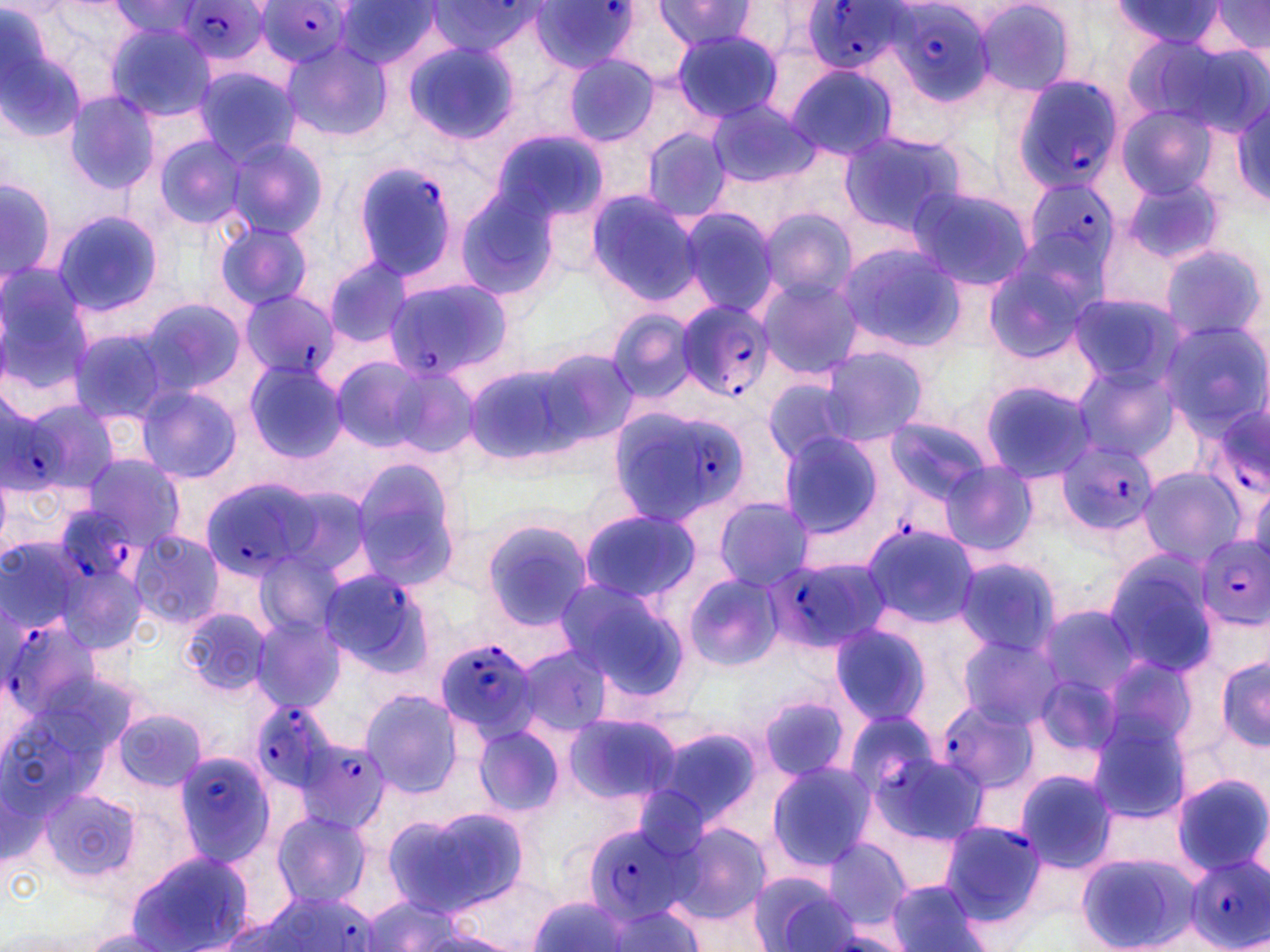

Summary:
  - Coordinate format: approximate bounding boxes as [x1, y1, x2, y2] in pixels
  - Plasmodium falciparum-infected red blood cell locations: [531, 0, 639, 72], [174, 1, 272, 68], [255, 1, 356, 67], [427, 1, 542, 57], [800, 1, 909, 76], [888, 2, 997, 105], [1010, 76, 1123, 196], [352, 160, 460, 286], [1019, 180, 1118, 279], [383, 279, 510, 382], [238, 289, 338, 383], [673, 299, 773, 400], [17, 398, 122, 495], [1222, 400, 1270, 504], [613, 404, 753, 527], [1055, 439, 1159, 535], [197, 478, 326, 582], [55, 506, 136, 583], [1197, 536, 1270, 626], [761, 557, 884, 657], [318, 567, 434, 677], [0, 612, 105, 735], [434, 638, 542, 738], [936, 696, 1035, 800], [252, 699, 339, 793], [849, 713, 937, 800], [295, 735, 390, 835], [174, 749, 279, 869], [941, 820, 1046, 924], [583, 823, 693, 921], [1185, 854, 1270, 949], [242, 891, 377, 952]
  - Uninfected red blood cell locations: [973, 0, 1078, 96], [1108, 0, 1224, 56], [111, 1, 210, 44], [334, 1, 436, 70], [653, 1, 758, 52], [1202, 1, 1270, 57], [0, 5, 88, 141], [604, 5, 700, 87], [105, 22, 218, 121], [671, 29, 783, 124], [1169, 38, 1270, 137], [402, 39, 519, 143], [281, 42, 392, 141], [560, 53, 663, 147], [785, 63, 898, 162], [192, 66, 301, 164], [64, 90, 161, 195], [1227, 95, 1270, 208], [707, 99, 820, 186], [1115, 104, 1218, 201], [638, 125, 735, 226], [490, 128, 607, 229], [837, 129, 967, 234], [157, 135, 246, 228], [226, 138, 326, 238], [1117, 171, 1228, 268], [0, 177, 57, 279], [905, 185, 1034, 292], [453, 186, 565, 301], [584, 189, 704, 305], [672, 206, 781, 317], [757, 208, 858, 304], [53, 211, 162, 316], [216, 222, 314, 311], [833, 243, 965, 355], [1160, 244, 1266, 343], [982, 249, 1098, 365], [323, 256, 412, 348], [0, 264, 94, 394], [755, 276, 864, 380], [1065, 292, 1182, 388], [138, 297, 246, 396], [605, 310, 703, 404], [1156, 320, 1269, 432], [66, 327, 174, 428], [532, 344, 642, 450], [816, 347, 929, 446], [329, 356, 429, 453], [244, 360, 349, 462], [465, 360, 586, 466], [381, 362, 482, 460], [1071, 364, 1181, 463], [761, 375, 860, 468], [980, 379, 1099, 482], [135, 384, 243, 484], [882, 416, 992, 507], [777, 433, 887, 538], [79, 453, 186, 549], [348, 458, 465, 592], [940, 461, 1040, 558], [1136, 466, 1246, 566], [269, 482, 378, 585], [712, 498, 817, 591], [579, 507, 700, 604], [480, 518, 593, 632], [861, 524, 982, 631], [127, 531, 225, 629], [3, 542, 83, 640], [252, 549, 345, 642], [56, 552, 151, 656], [1102, 553, 1218, 679], [953, 556, 1062, 660], [685, 573, 785, 672], [551, 576, 683, 691], [1034, 602, 1140, 706], [182, 607, 273, 698], [248, 615, 348, 714], [827, 624, 932, 726], [954, 632, 1065, 732], [510, 645, 615, 736], [1096, 652, 1205, 758], [1215, 653, 1269, 753], [359, 689, 466, 799], [757, 695, 853, 783], [113, 707, 207, 793], [563, 712, 683, 805], [1085, 715, 1194, 823], [473, 723, 565, 818], [650, 723, 765, 830], [765, 761, 874, 870], [1013, 768, 1118, 873], [1171, 774, 1269, 877], [39, 789, 140, 882], [393, 807, 531, 915], [272, 812, 373, 906], [667, 818, 772, 929], [818, 837, 917, 932], [126, 849, 257, 952], [1074, 852, 1201, 952], [749, 870, 861, 951], [885, 879, 988, 951], [531, 895, 632, 952], [359, 897, 490, 951], [603, 904, 704, 952], [71, 929, 179, 950]
  - Slide-level diagnosis: Plasmodium falciparum
  - Preparation: thin blood smear
  - Field of view: one of a larger specimen
  - Magnification: 1000x
  - Modality: light microscopy
  - Image size: 1270×952 pixels
  - Stain: May-Grünwald-Giemsa